Classify this cell by malaria status.
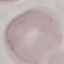

Uninfected.

Giemsa stain. Thin blood film. Acquired by smartphone through the microscope eyepiece. Cell patch, automatically extracted from a larger field of view and resized to 64 × 64 pixels.